Classify this cell by malaria status.
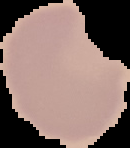
Uninfected.

Summary:
  - Image type: segmented cell region with the area outside set to black
  - Preparation: thin blood smear
  - Image size: 130×148 pixels